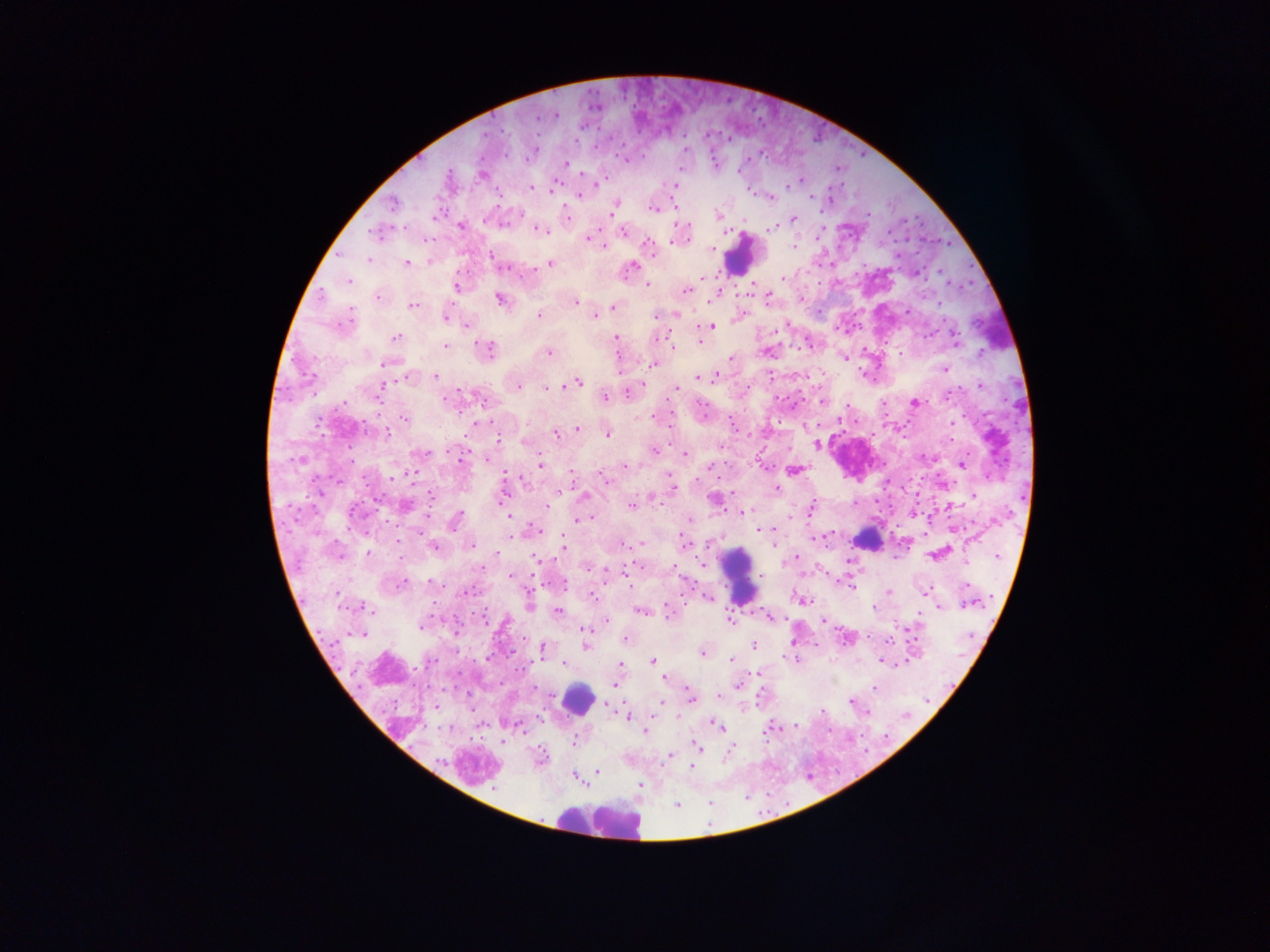
Approximate centers as x y in pixels.
Summary:
  - Plasmodium parasite locations: 555 115; 533 149; 624 159; 565 163; 678 169; 481 175; 799 180; 794 182; 597 183; 676 185; 529 187; 586 187; 553 189; 580 194; 770 196; 811 196; 828 201; 392 205; 613 206; 653 208; 717 215; 566 217; 793 219; 460 226; 773 227; 538 229; 623 231; 375 233; 588 237; 603 245; 648 246; 792 247; 711 250; 491 257; 368 259; 429 261; 406 263; 549 263; 632 266; 916 273; 703 278; 782 279; 348 280; 647 284; 457 286; 687 289; 378 296; 715 296; 766 298; 499 299; 800 300; 576 302; 413 304; 938 304; 614 306; 907 311; 539 315; 655 315; 677 315; 595 316; 739 316; 446 317; 344 323; 467 325; 711 326; 656 337; 396 338; 615 338; 955 340; 700 342; 809 344; 445 345; 673 345; 485 350; 768 350; 549 352; 900 352; 980 354; 730 358; 844 358; 388 363; 653 364; 944 369; 435 376; 408 377; 698 377; 713 378; 576 382; 980 385; 382 386; 518 386; 548 387; 638 388; 676 388; 628 391; 479 397; 605 397; 822 399; 915 402; 654 417; 405 418; 952 423; 805 426; 577 430; 385 433; 555 433; 607 434; 496 436; 526 441; 816 444; 720 447; 654 451; 421 452; 685 454; 489 458; 460 460; 962 464; 540 465; 625 466; 793 469; 570 473; 505 476; 604 478; 942 484; 672 488; 776 489; 558 490; 973 495; 583 496; 502 497; 652 497; 714 499; 631 504; 405 505; 546 506; 810 509; 743 512; 510 517; 590 517; 789 518; 582 519; 454 520; 687 521; 758 529; 536 530; 511 533; 815 537; 774 541; 563 542; 641 543; 684 543; 472 544; 433 545; 564 549; 367 553; 496 554; 936 555; 399 558; 796 558; 538 560; 703 564; 587 566; 672 568; 626 573; 511 576; 848 583; 397 585; 468 590; 888 591; 926 592; 591 596; 707 596; 803 600; 969 602; 528 603; 938 606; 364 608; 642 611; 557 612; 667 612; 768 617; 730 620; 823 620; 606 621; 422 623; 584 630; 359 634; 847 637; 624 639; 793 641; 585 645; 753 645; 815 645; 542 648; 701 652; 732 660; 795 660; 652 661; 881 662; 565 663; 620 664; 521 669; 759 673; 664 679; 615 684; 738 684; 874 688; 717 694; 690 696; 662 701; 851 701; 612 703; 677 716; 628 717; 650 717; 716 725; 795 725; 769 728; 646 731; 574 740; 698 748; 730 748; 667 755; 539 758; 693 766; 597 772; 575 776; 639 785; 677 806
  - Leukocyte locations: 740 254; 999 330; 868 539; 738 575; 577 699; 598 822
  - Image size: 1270×952 pixels
  - Capture: mobile-phone photograph through a microscope
  - Preparation: thick blood film
  - Field of view: single
  - Country: Ghana